Classify this cell by malaria status.
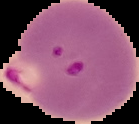
Parasitized.

preparation = thin blood smear
image type = cell region segmented out of the field of view; surrounding area masked to black
image size = 139×124 pixels